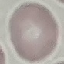
Result: negative for malaria parasites. Acquired by smartphone through the microscope eyepiece. Cell patch, automatically extracted from a larger field of view and resized to 64 × 64 pixels. Giemsa stain. Thin blood smear.